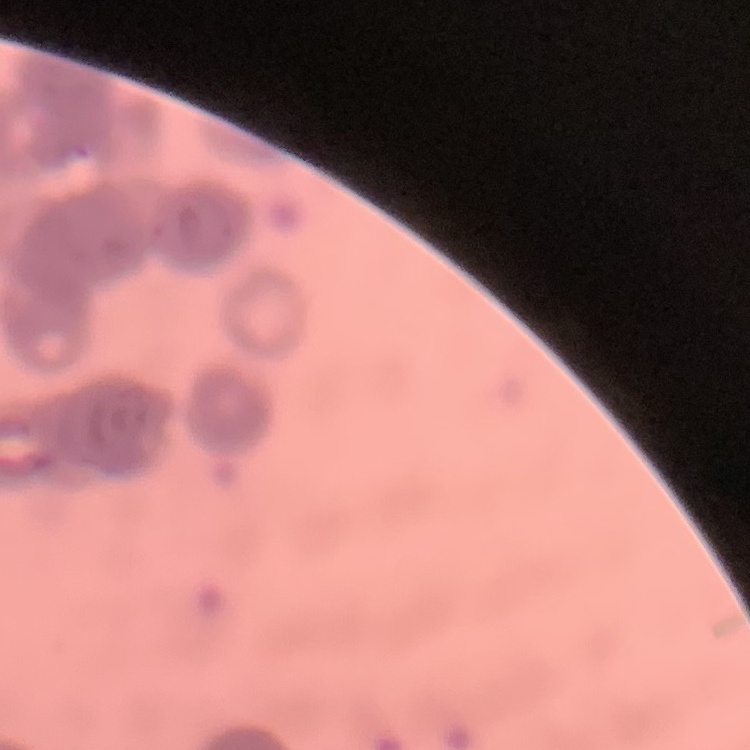
Summary:
  - Erythrocyte morphology: rouleaux formation
  - Stain: Field's or Giemsa
  - Image type: square crop of a larger photomicrograph
  - Preparation: thin blood smear